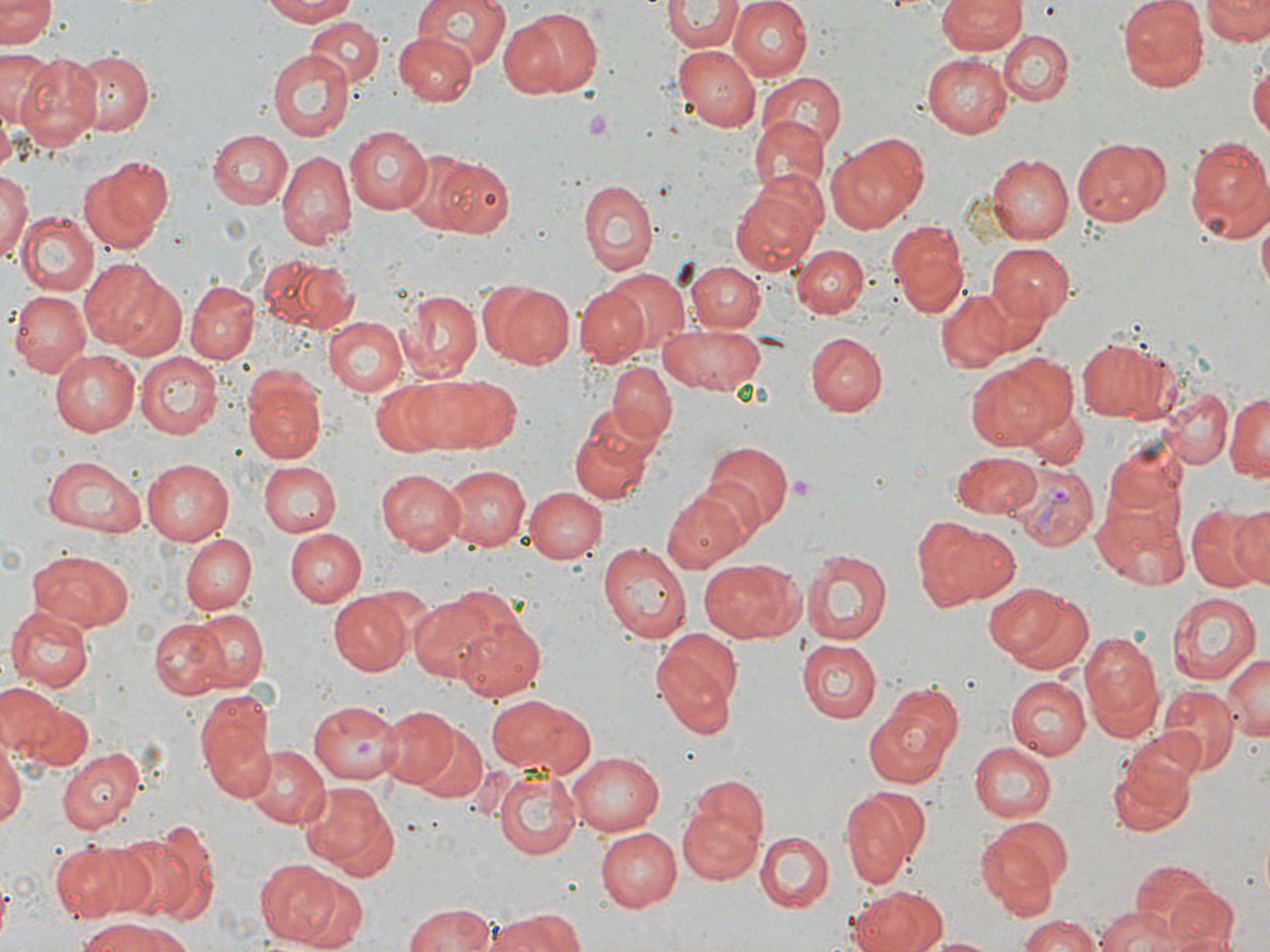
Summary:
  - Coordinate format: approximate bounding boxes as (x1, y1, x2, y2) in pixels
  - Platelet locations: (584, 111, 617, 139), (784, 474, 816, 502)
  - Uninfected red blood cell locations: (0, 0, 56, 50), (260, 0, 364, 24), (413, 0, 511, 73), (727, 0, 812, 81), (936, 0, 1024, 54), (1119, 0, 1209, 91), (1202, 0, 1270, 44), (664, 1, 742, 52), (503, 7, 597, 99), (305, 16, 383, 89), (1000, 31, 1074, 105), (392, 33, 476, 106), (673, 46, 761, 131), (0, 48, 53, 132), (266, 49, 353, 141), (67, 51, 155, 134), (15, 54, 104, 148), (921, 54, 1013, 137), (1250, 59, 1270, 145), (758, 73, 845, 151), (746, 114, 828, 205), (343, 124, 433, 215), (207, 129, 291, 209), (829, 132, 928, 230), (1182, 133, 1270, 244), (1072, 137, 1171, 226), (278, 150, 357, 248), (988, 152, 1074, 244), (423, 153, 515, 240), (77, 157, 170, 252), (0, 167, 30, 268), (579, 178, 657, 276), (730, 178, 823, 274), (13, 209, 97, 296), (1257, 212, 1269, 297), (888, 219, 969, 317), (985, 242, 1076, 323), (793, 244, 868, 319), (259, 254, 356, 332), (79, 258, 174, 354), (686, 258, 764, 333), (600, 269, 690, 357), (480, 279, 576, 373), (185, 280, 259, 362), (577, 286, 648, 367), (936, 288, 1015, 372), (8, 290, 92, 377), (400, 290, 482, 381), (327, 315, 409, 396), (657, 323, 767, 395), (805, 331, 887, 417), (1075, 334, 1183, 423), (48, 348, 140, 436), (136, 353, 224, 438), (964, 357, 1068, 454), (607, 361, 677, 443), (407, 376, 518, 451), (246, 377, 327, 463), (371, 382, 451, 455), (1161, 388, 1232, 467), (1225, 391, 1270, 485), (1024, 408, 1087, 467), (570, 415, 656, 503), (702, 438, 793, 532), (1101, 440, 1192, 528), (951, 451, 1043, 517), (41, 455, 147, 536), (140, 458, 237, 544), (256, 460, 339, 537), (440, 464, 530, 550), (376, 468, 466, 553), (523, 486, 606, 564), (663, 489, 751, 574), (1092, 501, 1192, 588), (1187, 502, 1270, 593), (1229, 505, 1270, 585), (929, 523, 1022, 607), (283, 528, 366, 606), (180, 534, 257, 615), (597, 541, 693, 643), (800, 546, 892, 648), (28, 549, 135, 634), (698, 560, 802, 642), (982, 580, 1089, 672), (329, 590, 414, 675), (1165, 590, 1261, 685), (409, 597, 502, 682), (6, 606, 93, 691), (187, 608, 269, 692), (451, 613, 546, 702), (147, 616, 231, 700), (1081, 629, 1164, 735), (651, 630, 742, 737), (797, 640, 881, 723), (1222, 654, 1268, 742), (1006, 676, 1090, 759), (0, 682, 63, 759), (1157, 686, 1238, 773), (862, 689, 964, 787), (197, 693, 277, 805), (485, 694, 596, 778), (307, 700, 401, 783), (23, 702, 90, 769), (379, 706, 459, 788), (411, 722, 487, 804), (0, 738, 24, 836), (969, 742, 1055, 821), (246, 745, 328, 829), (56, 746, 145, 833), (568, 752, 666, 835), (1109, 754, 1196, 838), (491, 768, 582, 859), (298, 779, 400, 878), (841, 786, 929, 888), (677, 795, 766, 881), (976, 824, 1066, 918), (595, 827, 681, 910), (116, 828, 213, 924), (756, 832, 834, 911), (54, 841, 150, 923), (255, 858, 338, 946), (1133, 862, 1218, 937), (294, 873, 366, 950), (1166, 886, 1237, 952), (849, 888, 945, 952), (401, 903, 501, 952), (1093, 908, 1180, 952), (487, 909, 583, 952), (1017, 916, 1103, 952), (76, 918, 191, 952), (918, 935, 1005, 952)
  - Plasmodium vivax-infected red blood cell locations: (1011, 464, 1098, 550)
  - Slide-level diagnosis: Plasmodium vivax
  - Magnification: 1000x
  - Preparation: thin blood smear
  - Stain: May-Grünwald-Giemsa
  - Field of view: one of a larger specimen
  - Image size: 1270×952 pixels
  - Modality: light microscopy